Classify this cell by malaria status.
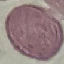
It is uninfected.

Cell patch, automatically extracted from a larger field of view and resized to 64 × 64 pixels. Giemsa-stained preparation. Acquired by smartphone through the microscope eyepiece. Thin smear of blood.